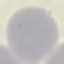

Summary:
  - Result: no malaria parasites seen
  - Stain: Giemsa
  - Image type: automatically extracted cell patch, resized to 64 × 64 pixels
  - Capture: smartphone camera at the microscope eyepiece
  - Preparation: thin blood smear